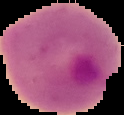

malaria status = parasitized
image type = cell region segmented out of the field of view; surrounding area masked to black
image size = 124×115 pixels
preparation = thin blood film